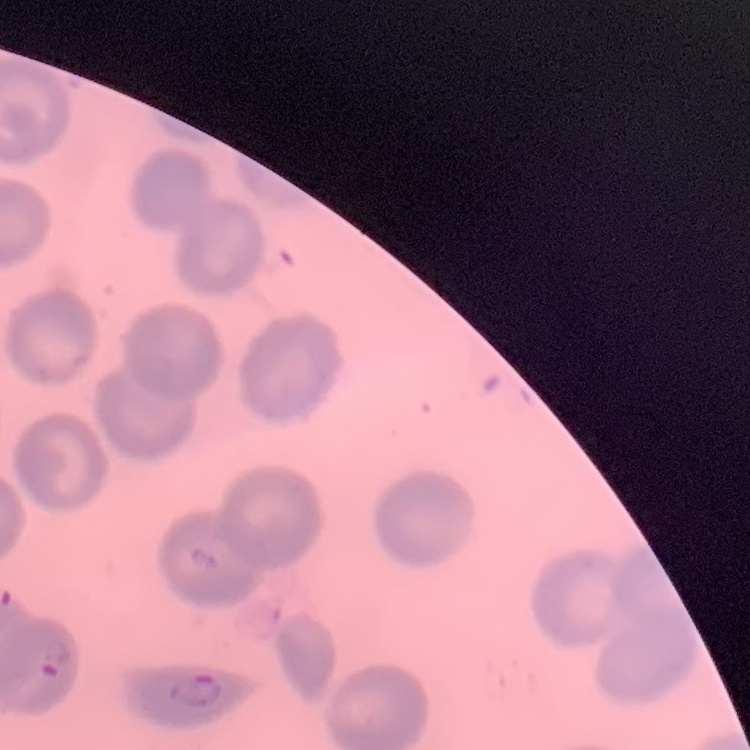
{
  "erythrocyte_morphology": "no rouleaux formation",
  "stain": "Field's or Giemsa",
  "preparation": "thin blood smear",
  "image_type": "one tile cut from a larger photomicrograph"
}